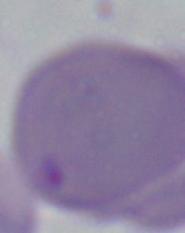
Micrograph. A Babesia parasite is seen. 1000x magnification.